Classify this cell by malaria status.
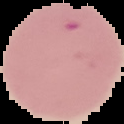

Parasitized.

image size = 124×124 pixels
image type = segmented cell region on a black background
preparation = thin blood film